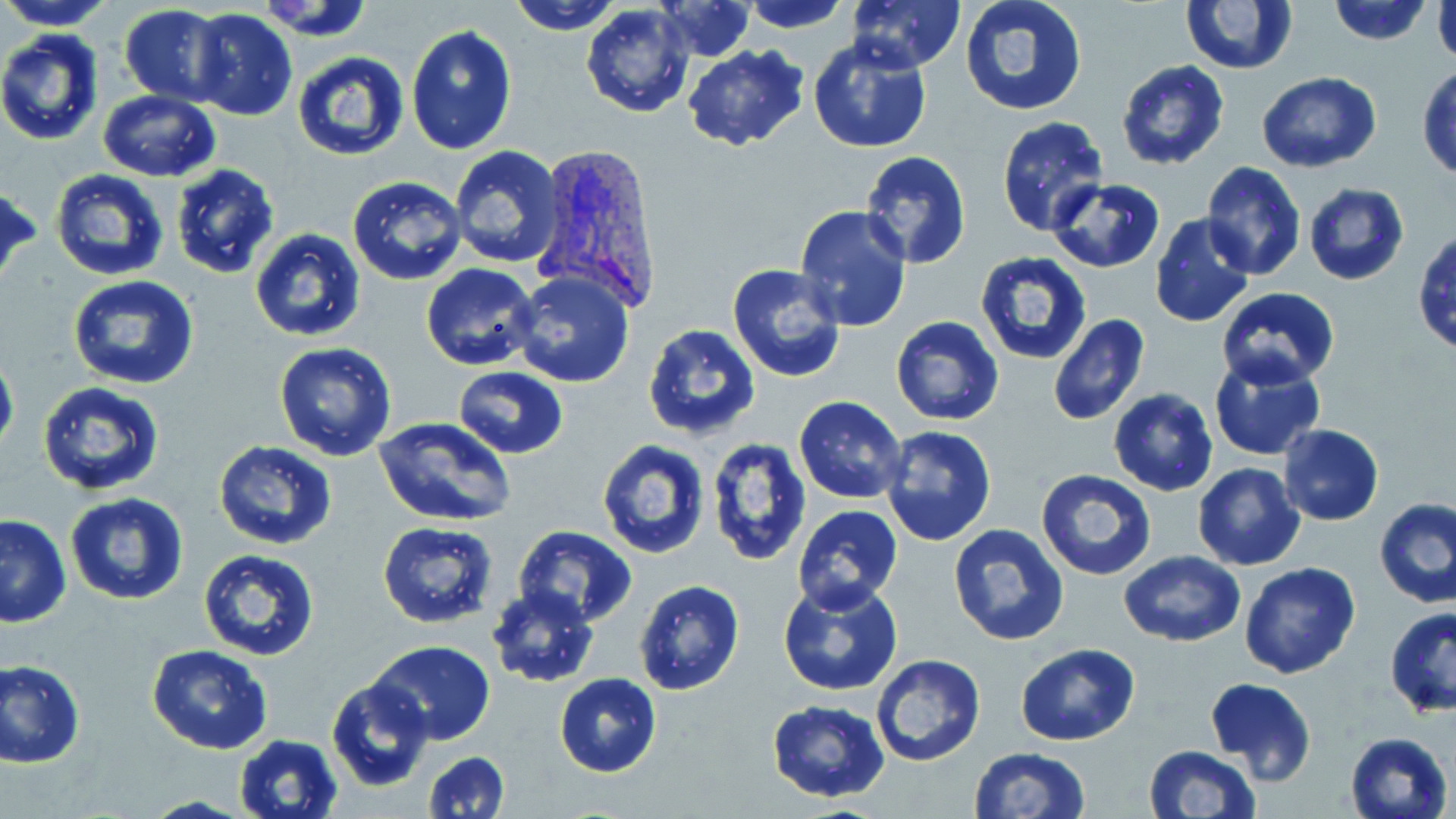
Summary:
  - Coordinate format: approximate bounding boxes as named x1/y1/x2/y2 corners in pixels
  - Plasmodium vivax-infected red blood cell locations: (x1=531, y1=145, x2=663, y2=312)
  - Uninfected red blood cell locations: (x1=0, y1=0, x2=116, y2=29), (x1=508, y1=0, x2=621, y2=35), (x1=654, y1=0, x2=754, y2=61), (x1=740, y1=0, x2=851, y2=32), (x1=846, y1=0, x2=966, y2=75), (x1=959, y1=0, x2=1089, y2=116), (x1=1328, y1=0, x2=1433, y2=46), (x1=1181, y1=1, x2=1296, y2=74), (x1=581, y1=2, x2=696, y2=118), (x1=1431, y1=2, x2=1455, y2=64), (x1=120, y1=4, x2=228, y2=106), (x1=188, y1=10, x2=297, y2=123), (x1=405, y1=25, x2=517, y2=156), (x1=0, y1=28, x2=104, y2=146), (x1=807, y1=36, x2=932, y2=154), (x1=683, y1=44, x2=810, y2=153), (x1=293, y1=51, x2=411, y2=162), (x1=1116, y1=60, x2=1229, y2=170), (x1=1416, y1=65, x2=1456, y2=179), (x1=1259, y1=72, x2=1382, y2=172), (x1=98, y1=91, x2=221, y2=182), (x1=996, y1=116, x2=1107, y2=236), (x1=447, y1=145, x2=565, y2=268), (x1=860, y1=150, x2=972, y2=269), (x1=1200, y1=160, x2=1306, y2=281), (x1=170, y1=163, x2=280, y2=279), (x1=49, y1=168, x2=169, y2=282), (x1=347, y1=175, x2=469, y2=285), (x1=1047, y1=178, x2=1167, y2=273), (x1=1301, y1=182, x2=1410, y2=286), (x1=0, y1=184, x2=41, y2=290), (x1=794, y1=204, x2=913, y2=331), (x1=1147, y1=213, x2=1255, y2=328), (x1=248, y1=229, x2=369, y2=344), (x1=1412, y1=231, x2=1456, y2=359), (x1=974, y1=253, x2=1091, y2=366), (x1=420, y1=263, x2=542, y2=372), (x1=726, y1=263, x2=849, y2=383), (x1=510, y1=272, x2=636, y2=389), (x1=66, y1=274, x2=200, y2=390), (x1=1216, y1=287, x2=1340, y2=387), (x1=890, y1=315, x2=1004, y2=425), (x1=1047, y1=315, x2=1149, y2=425), (x1=642, y1=323, x2=760, y2=439), (x1=274, y1=342, x2=398, y2=462), (x1=0, y1=349, x2=19, y2=460), (x1=1208, y1=355, x2=1326, y2=459), (x1=453, y1=366, x2=569, y2=459), (x1=37, y1=382, x2=165, y2=496), (x1=1108, y1=388, x2=1218, y2=495), (x1=794, y1=395, x2=908, y2=504), (x1=374, y1=417, x2=516, y2=527), (x1=1277, y1=424, x2=1385, y2=526), (x1=880, y1=426, x2=998, y2=547), (x1=706, y1=437, x2=813, y2=567), (x1=597, y1=438, x2=710, y2=560), (x1=213, y1=439, x2=339, y2=551), (x1=1192, y1=463, x2=1305, y2=570), (x1=1037, y1=469, x2=1157, y2=582), (x1=65, y1=493, x2=190, y2=606), (x1=1374, y1=499, x2=1456, y2=608), (x1=793, y1=504, x2=903, y2=612), (x1=0, y1=515, x2=72, y2=628), (x1=377, y1=520, x2=499, y2=630), (x1=946, y1=523, x2=1069, y2=646), (x1=513, y1=527, x2=639, y2=628), (x1=197, y1=549, x2=320, y2=662), (x1=1119, y1=551, x2=1245, y2=646), (x1=1238, y1=561, x2=1362, y2=679), (x1=632, y1=579, x2=744, y2=697), (x1=777, y1=579, x2=904, y2=697), (x1=485, y1=584, x2=599, y2=687), (x1=1384, y1=607, x2=1456, y2=718), (x1=365, y1=641, x2=495, y2=745), (x1=1015, y1=642, x2=1141, y2=746), (x1=146, y1=644, x2=272, y2=754), (x1=870, y1=655, x2=987, y2=768), (x1=1, y1=659, x2=85, y2=767), (x1=554, y1=673, x2=662, y2=777), (x1=325, y1=677, x2=435, y2=792), (x1=1204, y1=677, x2=1317, y2=786), (x1=765, y1=700, x2=890, y2=802), (x1=1345, y1=730, x2=1452, y2=818), (x1=233, y1=735, x2=344, y2=819), (x1=1143, y1=744, x2=1262, y2=819), (x1=970, y1=745, x2=1090, y2=819), (x1=425, y1=750, x2=510, y2=819), (x1=137, y1=796, x2=258, y2=819)
  - Slide-level diagnosis: Plasmodium vivax
  - Stain: May-Grünwald-Giemsa
  - Preparation: thin blood film
  - Magnification: 1000x
  - Field of view: single
  - Image size: 1456×819 pixels
  - Modality: light microscopy